Evaluate for malaria.
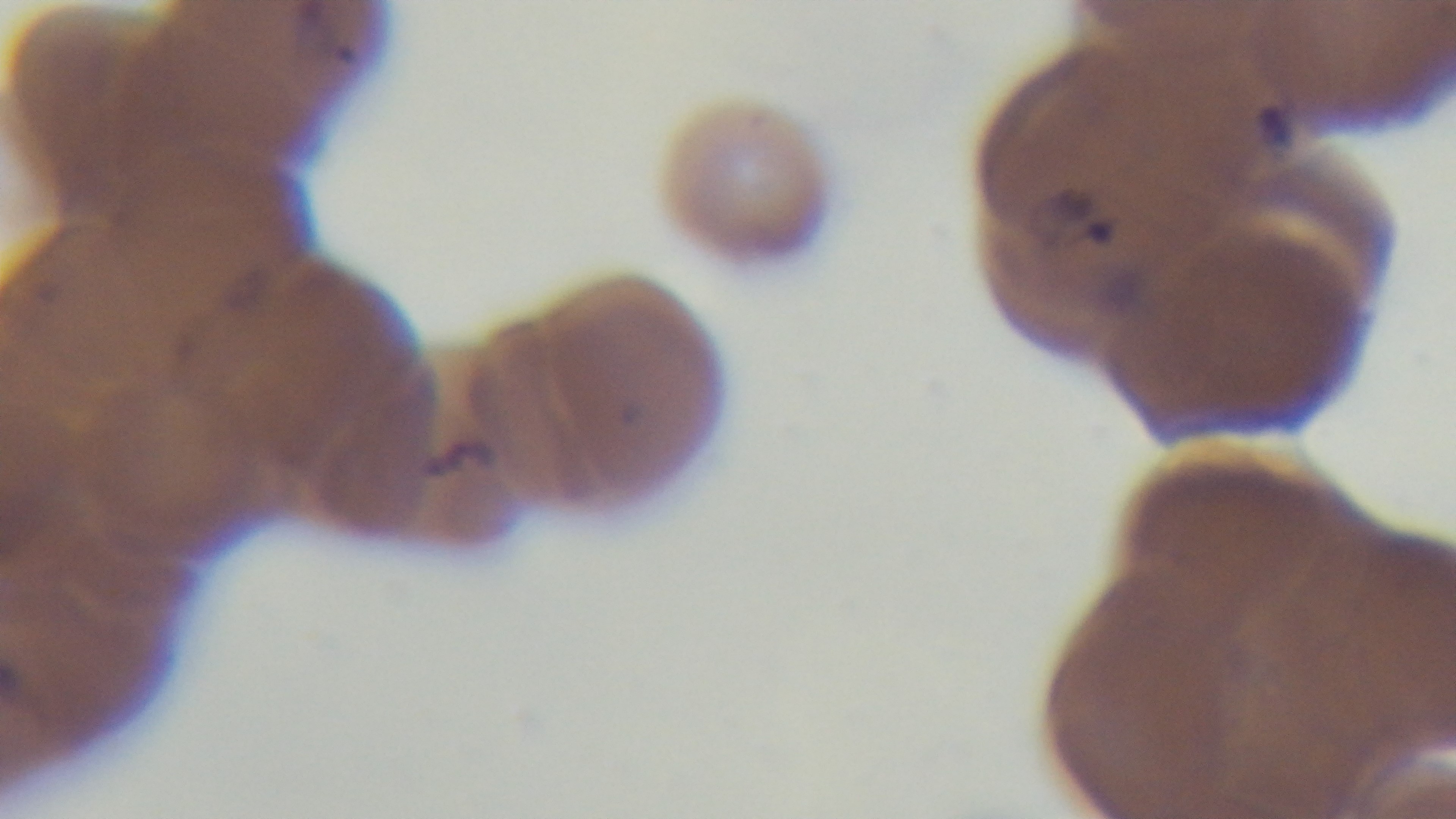

Positive.

One field from the slide. Light microscopy. Oil-immersion objective, 100x. Preparation: thin smear. Captured with a mounted 4K digital camera. Giemsa-stained.